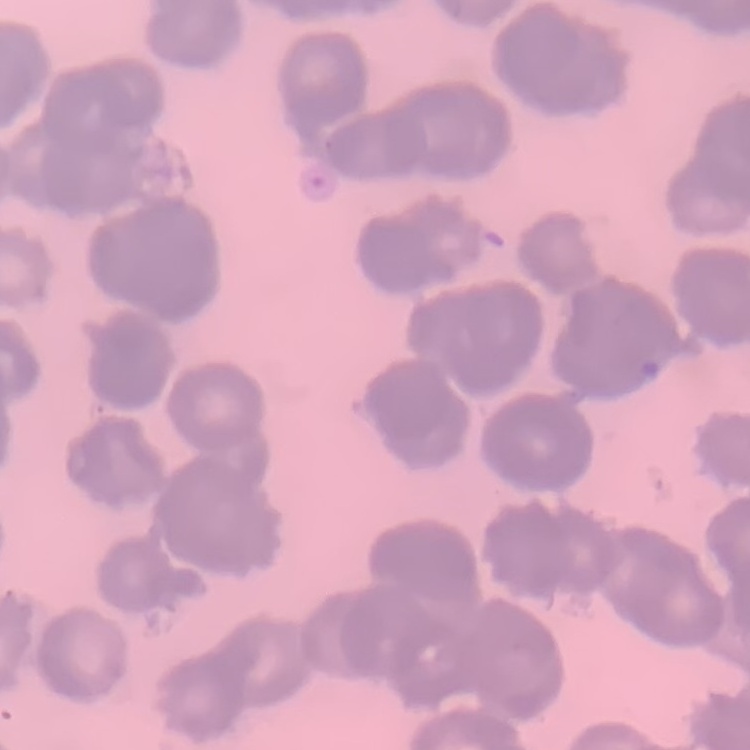
red blood cell morphology = rouleaux formation
preparation = thin blood smear
stain = Field's or Giemsa
image type = square crop of a larger photomicrograph